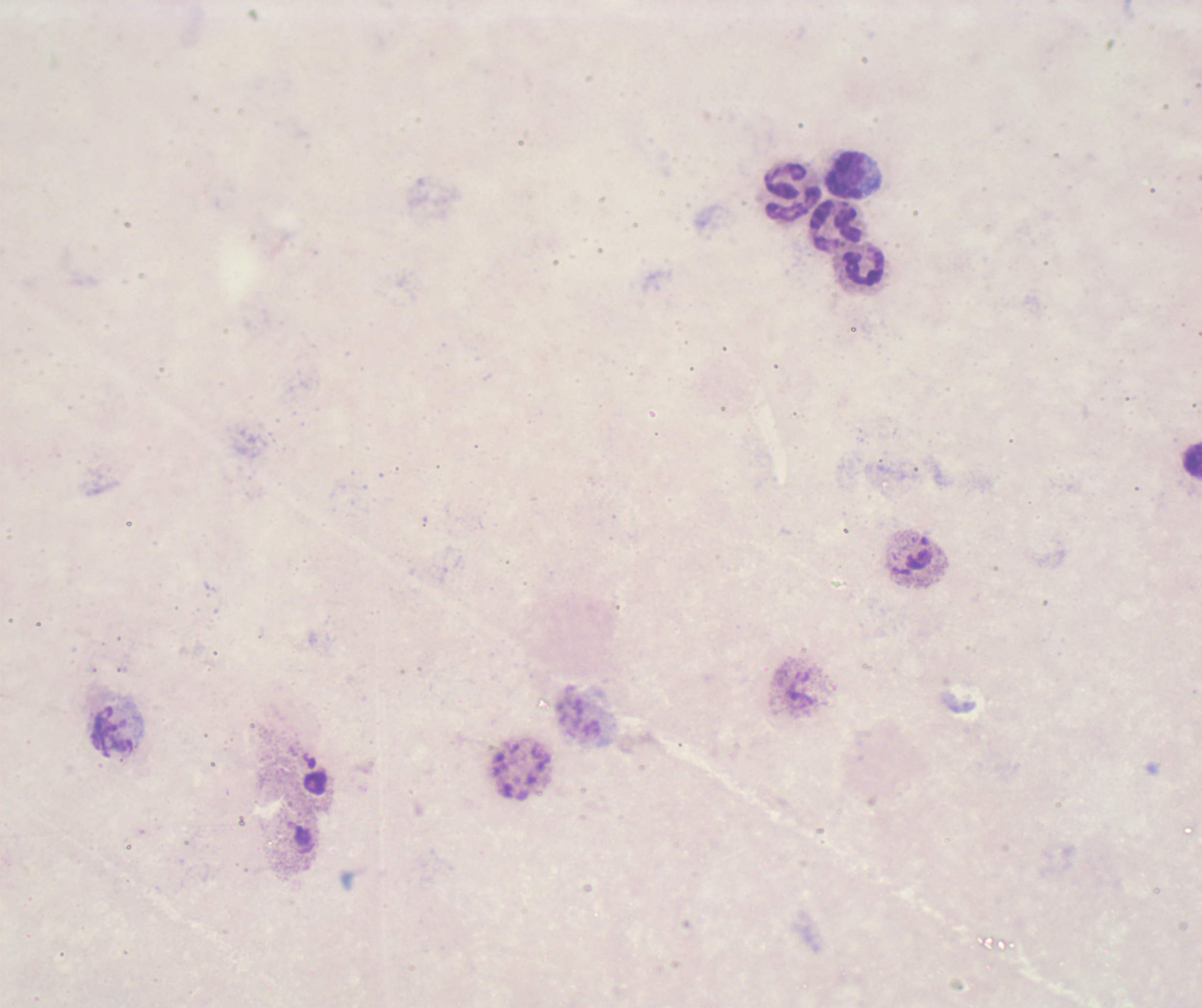
Approximate centers as [x, y] in pixels. Leukocyte locations: [846, 175], [792, 193], [837, 226], [865, 267], [1192, 461], [114, 731]. Thick blood film. Romanowsky stain. Captured at 100x magnification. Background quality: poor. Result: no malaria parasites seen. Image is 1202×1008 pixels. Previously used in a real diagnosis. One field from this slide. Coloration quality: bad.